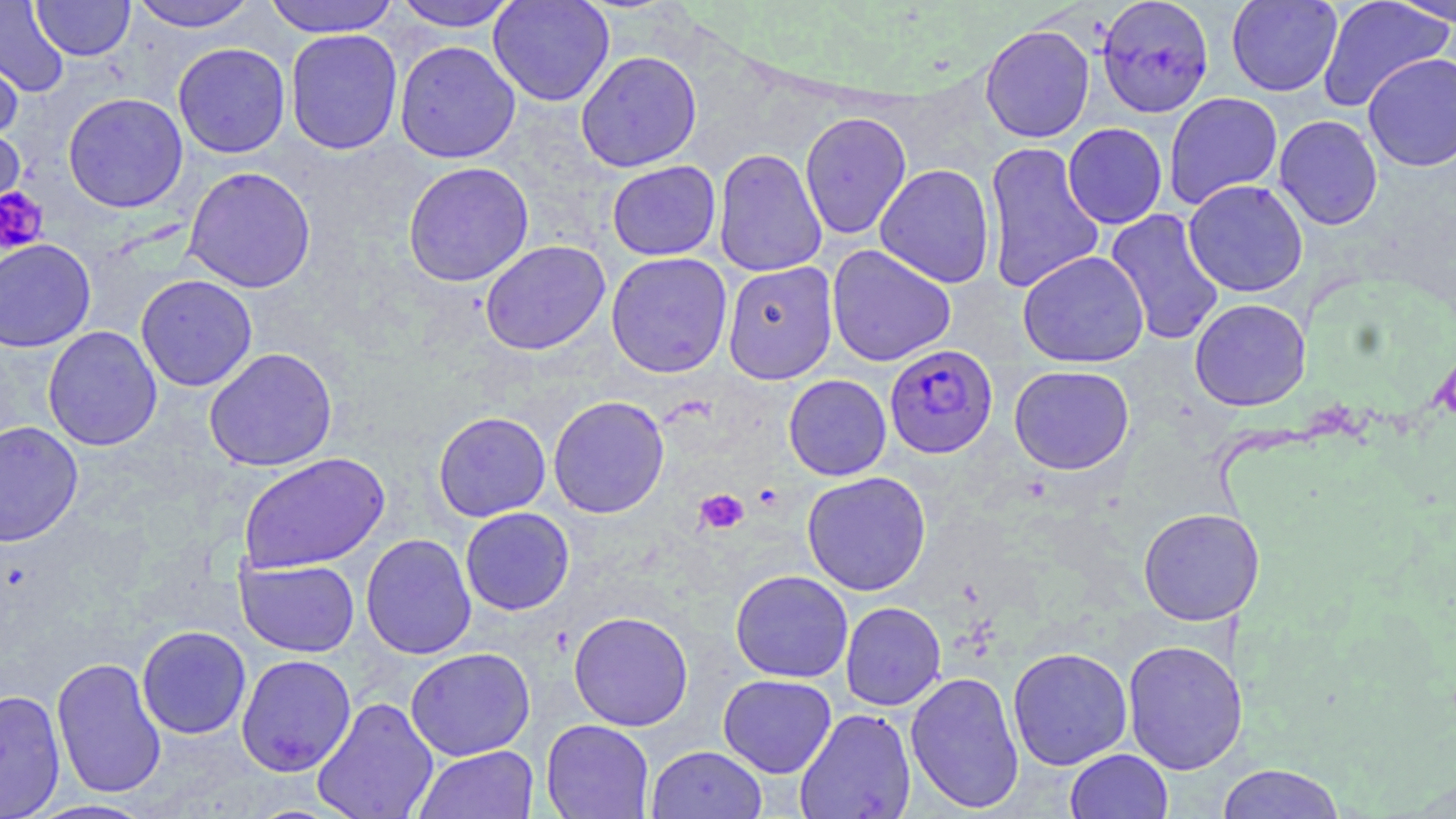
Approximate bounding boxes as [x1, y1, x2, y2] in pixels. Platelet locations: [1, 187, 48, 254], [754, 484, 784, 511], [694, 488, 749, 535]. Plasmodium falciparum-infected red blood cell locations: [885, 344, 999, 458]. Uninfected red blood cell locations: [263, 0, 399, 37], [392, 0, 520, 32], [488, 0, 615, 106], [1097, 0, 1216, 118], [1226, 0, 1342, 96], [1317, 0, 1453, 112], [1386, 0, 1456, 29], [0, 1, 68, 97], [31, 1, 135, 61], [128, 1, 260, 32], [980, 24, 1095, 143], [285, 29, 403, 155], [394, 40, 521, 163], [172, 43, 291, 158], [0, 47, 24, 147], [575, 50, 702, 172], [1362, 52, 1456, 172], [1164, 91, 1283, 208], [62, 92, 188, 213], [799, 111, 911, 240], [1273, 115, 1383, 230], [1062, 123, 1167, 229], [0, 125, 26, 229], [983, 141, 1105, 295], [713, 148, 828, 276], [607, 160, 721, 261], [403, 161, 534, 287], [874, 163, 996, 288], [183, 166, 316, 293], [1183, 179, 1308, 298], [1104, 208, 1226, 345], [0, 238, 96, 353], [480, 240, 610, 356], [826, 244, 956, 367], [1017, 250, 1149, 368], [606, 252, 733, 378], [722, 261, 838, 383], [135, 274, 257, 392], [1189, 298, 1311, 411], [43, 326, 162, 451], [205, 347, 338, 471], [1008, 365, 1134, 474], [783, 374, 892, 480], [548, 395, 670, 519], [433, 411, 551, 522], [0, 421, 83, 546], [238, 452, 390, 573], [801, 471, 932, 596], [460, 507, 575, 615], [1137, 507, 1265, 625], [360, 533, 477, 659], [235, 558, 359, 657], [730, 569, 853, 683], [840, 601, 946, 710], [568, 610, 693, 731], [136, 625, 252, 739], [1122, 639, 1248, 774], [405, 647, 535, 761], [1007, 647, 1133, 770], [235, 654, 357, 777], [51, 656, 167, 799], [905, 670, 1024, 813], [718, 673, 837, 777], [0, 689, 66, 819], [312, 696, 438, 819], [795, 708, 916, 819], [541, 719, 654, 818], [413, 745, 539, 819], [647, 745, 767, 818], [1064, 748, 1173, 819], [1215, 763, 1346, 819], [25, 799, 159, 818]. Slide-level diagnosis: Plasmodium falciparum. 1000x magnification. One field of a larger specimen. Light microscopy. Thin blood smear. May-Grünwald-Giemsa stain. Image is 1456×819 pixels.